Give the position of every malaria parasite and every leukocyte.
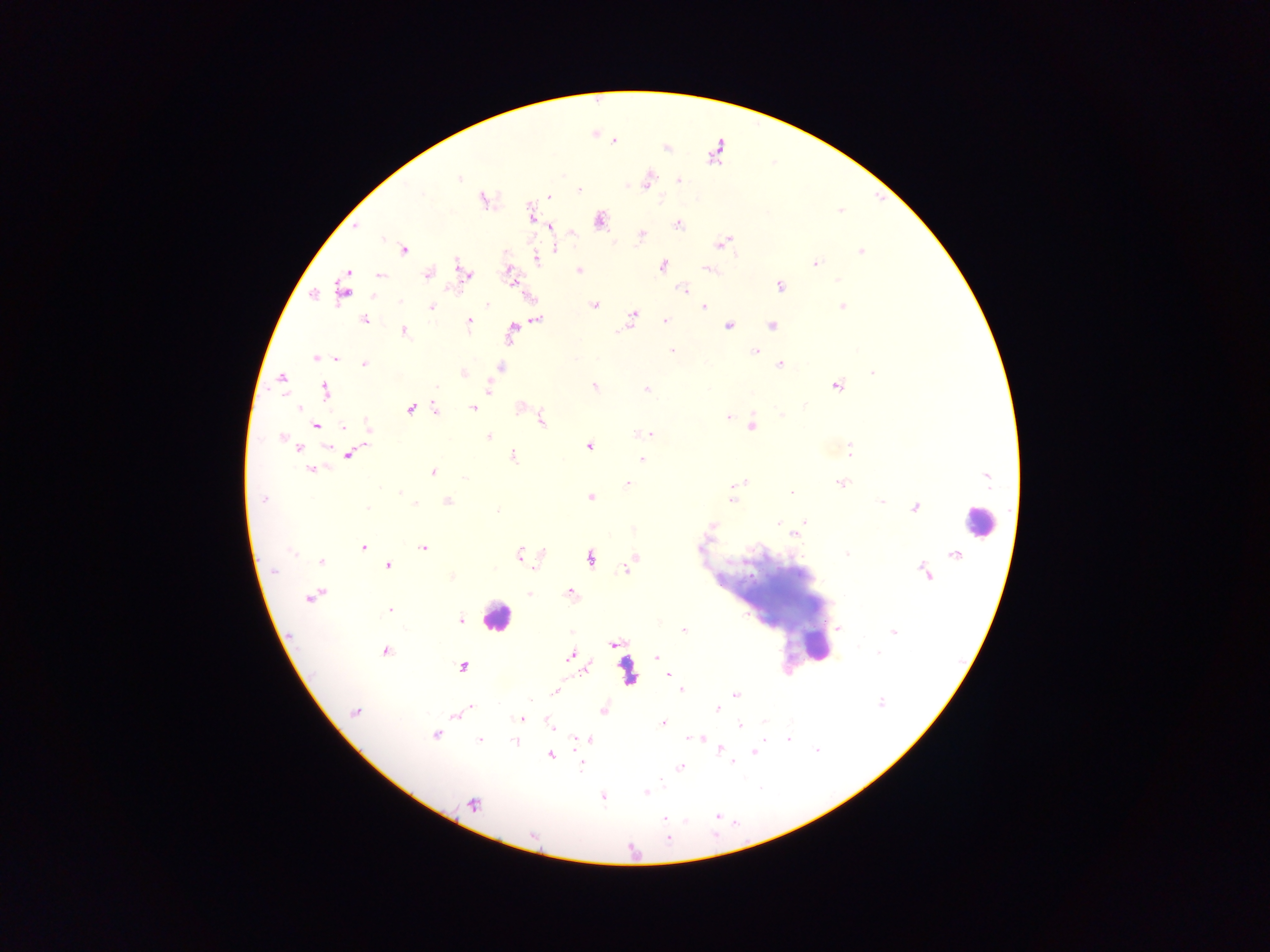

Approximate centers as x y in pixels.
Malaria parasites: 615 141; 459 179; 648 180; 678 180; 579 190; 549 196; 483 199; 530 210; 600 220; 678 224; 355 227; 551 227; 642 234; 724 242; 555 248; 403 250; 861 252; 537 260; 815 263; 457 264; 663 266; 710 270; 578 271; 428 274; 466 274; 380 275; 508 275; 838 279; 780 286; 683 289; 342 291; 528 296; 400 301; 487 304; 594 305; 432 307; 704 307; 842 307; 633 315; 364 320; 537 320; 665 320; 470 321; 729 325; 771 325; 512 329; 404 331; 672 350; 755 351; 316 358; 335 358; 364 364; 780 365; 501 367; 464 373; 872 373; 281 378; 837 385; 594 386; 436 388; 325 389; 488 389; 646 389; 804 405; 298 407; 473 408; 519 408; 410 409; 435 410; 782 414; 728 417; 541 420; 316 425; 343 426; 750 426; 368 428; 639 434; 649 434; 488 436; 281 437; 328 447; 589 447; 300 448; 850 450; 348 455; 514 456; 641 459; 311 469; 432 472; 464 477; 628 484; 742 484; 841 484; 734 485; 400 492; 791 492; 590 497; 264 499; 732 500; 448 501; 881 501; 415 504; 368 508; 914 508; 497 510; 805 522; 778 524; 711 526; 794 534; 363 547; 424 548; 291 552; 519 553; 847 554; 590 558; 633 559; 321 561; 388 566; 626 569; 274 571; 451 576; 529 593; 570 593; 310 597; 390 610; 460 620; 838 628; 683 630; 893 632; 613 643; 385 652; 879 652; 570 656; 657 657; 463 667; 586 669; 669 674; 681 690; 554 692; 735 694; 881 703; 471 707; 717 708; 604 710; 355 713; 456 714; 521 719; 662 724; 550 725; 739 725; 435 735; 701 738; 765 738; 589 739; 688 739; 788 739; 479 740; 576 740; 515 742; 720 748; 817 750; 753 751; 551 755; 733 763; 581 766; 680 767; 662 780; 662 784; 646 792; 602 796; 473 804; 716 816; 664 818; 668 839.
Leukocytes: 979 522; 496 617; 816 646.

Thick blood film. One field of view. Sample from Ghana. Photographed through a microscope with a mobile-phone camera. Image is 1270×952 pixels.